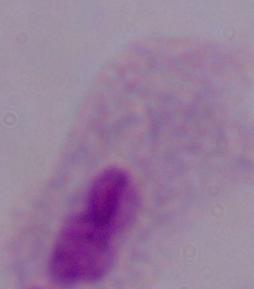
modality: photomicrograph
magnification: 1000x
identification: trichomonad